Point out each leukocyte.
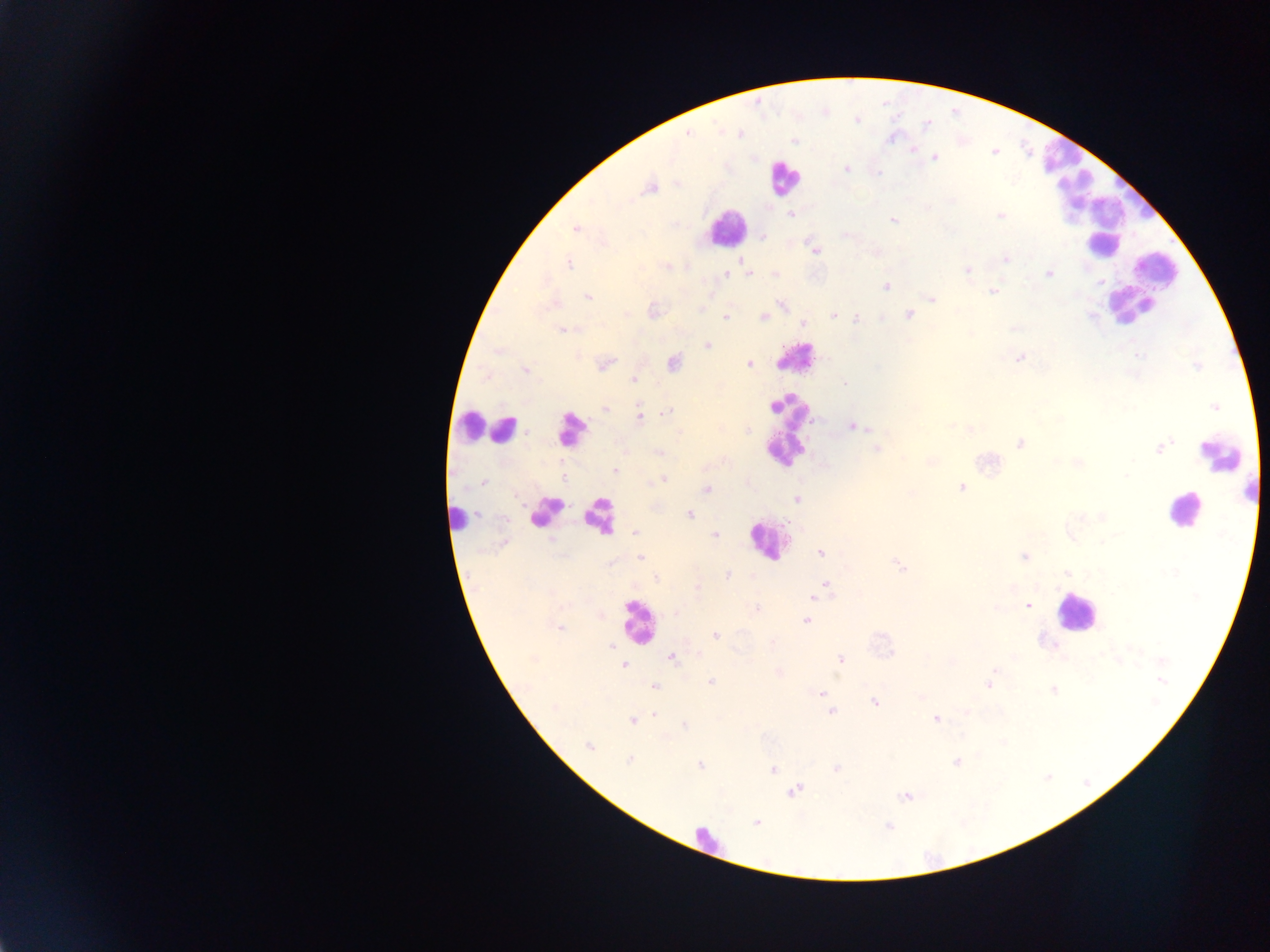
Approximate centers as x y in pixels.
Leukocytes: 1062 157; 782 178; 1074 192; 1088 205; 726 228; 1103 244; 1158 269; 1143 290; 1133 306; 796 358; 471 425; 488 427; 504 429; 570 430; 789 430; 1222 453; 1184 510; 545 512; 599 516; 458 519; 766 540; 1075 611; 638 622; 707 838.

Plasmodium parasite locations: 925 125; 687 132; 741 133; 794 140; 913 149; 934 157; 845 168; 650 186; 792 213; 1001 215; 893 219; 575 228; 846 234; 761 235; 814 249; 875 251; 742 258; 1005 258; 569 263; 666 266; 968 268; 1049 273; 748 274; 775 274; 724 275; 886 286; 992 291; 587 296; 932 297; 782 304; 702 310; 834 314; 908 314; 725 317; 763 317; 856 318; 803 322; 1013 328; 563 329; 707 344; 1019 358; 604 362; 673 362; 749 363; 525 369; 635 378; 845 384; 1215 407; 605 409; 666 413; 638 415; 851 425; 970 428; 1020 443; 876 448; 1160 448; 659 453; 929 461; 1077 463; 614 471; 662 479; 482 482; 961 487; 706 489; 797 499; 690 514; 635 532; 715 534; 503 543; 820 552; 1025 556; 640 557; 898 565; 1068 573; 726 576; 655 577; 827 585; 696 587; 820 593; 813 597; 1026 606; 755 608; 598 613; 675 613; 806 621; 559 627; 716 635; 608 647; 671 657; 841 660; 623 664; 993 669; 778 673; 711 682; 989 686; 654 687; 1053 689; 820 691; 922 696; 875 702; 964 710; 831 711; 655 716; 632 719; 936 719; 685 725; 589 747; 630 759; 957 762; 700 764; 837 768; 772 770; 794 791; 905 796; 757 822; 888 827. Single field of view. Image is 1270×952 pixels. Sample from Ghana. Thick blood smear. Mobile-phone photograph taken through the microscope.